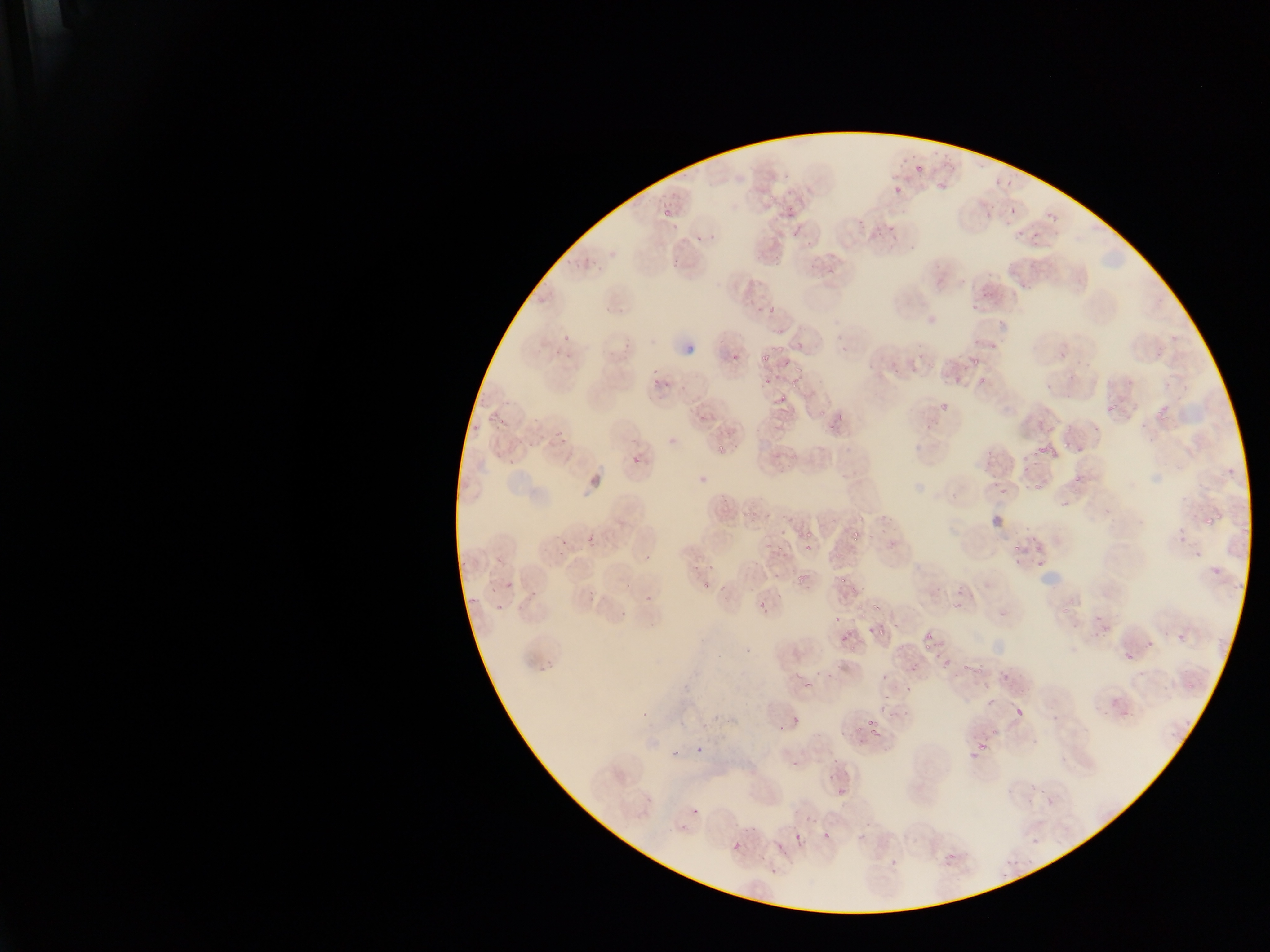
Approximate bounding boxes as left top right bottom in pixels. Plasmodium parasite locations: 913 161 927 175; 994 174 1006 183; 1005 178 1016 190; 936 180 949 191; 893 187 902 196; 1007 203 1021 214; 661 207 668 218; 787 209 795 216; 983 211 999 221; 1046 217 1058 228; 857 220 865 228; 890 223 897 232; 1033 228 1048 238; 1017 230 1025 237; 696 235 704 242; 711 235 719 240; 807 236 818 244; 670 252 684 270; 809 255 823 268; 825 266 835 278; 1023 278 1035 289; 971 290 991 309; 771 303 780 310; 995 319 1009 328; 973 335 981 346; 560 336 570 344; 992 341 997 349; 732 347 744 363; 771 347 781 355; 1059 351 1066 359; 759 355 771 365; 971 358 976 367; 783 361 793 369; 794 367 805 374; 765 375 778 388; 977 377 988 385; 653 378 661 385; 790 379 801 390; 777 394 787 407; 939 400 948 410; 480 402 487 410; 1105 404 1118 412; 835 414 845 423; 698 416 706 424; 827 419 839 430; 492 420 505 432; 924 423 931 431; 554 431 562 440; 558 438 566 444; 1062 440 1069 448; 529 442 538 449; 494 445 508 462; 1039 447 1048 455; 1050 447 1060 457; 1019 450 1030 461; 631 456 640 466; 509 461 518 466; 1074 474 1081 482; 1031 481 1039 490; 999 487 1007 493; 1062 500 1068 510; 880 511 892 519; 1216 513 1225 519; 1205 517 1216 526; 800 527 816 537; 852 529 861 543; 583 534 599 553; 762 537 774 549; 775 542 784 554; 888 542 896 547; 806 545 814 550; 1035 545 1041 553; 644 552 652 561; 1035 556 1043 565; 693 564 702 571; 771 570 783 578; 1212 570 1222 578; 795 572 809 589; 506 580 515 590; 624 581 635 588; 703 582 713 588; 488 586 494 596; 955 588 966 597; 776 589 787 598; 530 590 536 598; 588 594 598 602; 646 596 655 603; 466 597 475 608; 754 601 768 611; 497 602 505 608; 872 603 880 618; 620 610 629 619; 834 614 844 620; 866 625 875 635; 875 628 886 637; 839 633 849 642; 1177 633 1187 643; 922 635 933 643; 924 643 932 651; 1124 651 1133 659; 538 656 556 669; 940 660 956 670; 975 666 989 677; 793 672 804 678; 804 681 814 689; 904 686 916 694; 985 696 996 706; 1120 706 1130 713; 793 713 801 724; 867 719 878 731; 854 728 863 736; 872 728 882 742; 697 741 709 751; 979 741 988 749; 671 747 679 759; 969 750 984 759; 832 757 840 765; 824 774 835 781; 836 785 850 798; 692 809 699 818; 823 831 831 839; 794 833 804 842; 732 841 741 850; 777 842 786 851; 946 852 959 863; 891 859 899 867 | approximate x y pixel centers of objects too small to bound: 879 233; 654 371; 667 386; 721 447; 988 452; 1024 472; 860 518; 881 531; 1035 538; 564 541; 1017 548; 711 570; 844 580; 1098 617; 965 666; 1018 712; 645 714; 793 765; 1044 790; 682 828; 1037 840. Thin blood film. Photographed through a microscope with a mobile-phone camera. One field of view. Image is 1270×952 pixels. Collected in Ghana.